Comment on the morphology of the erythrocytes.
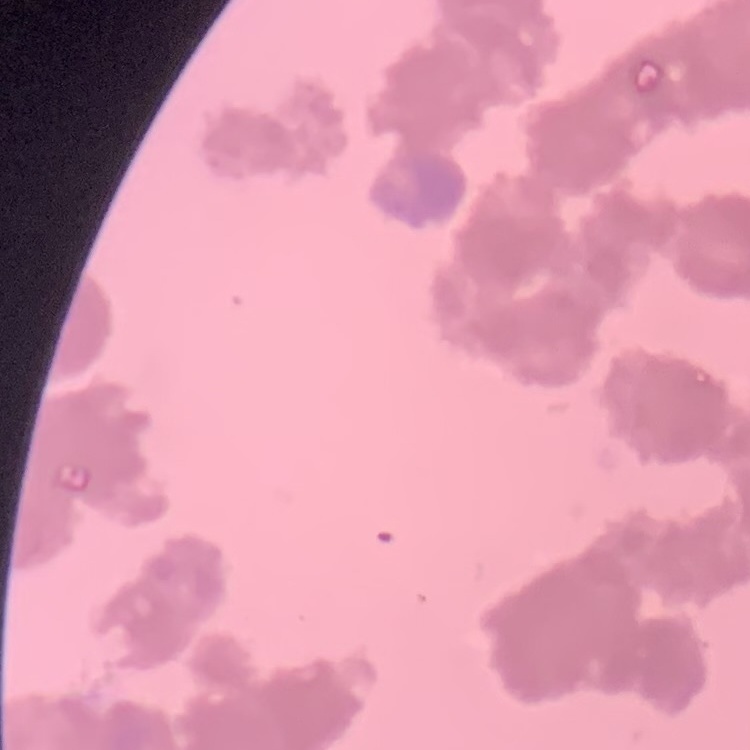
They show rouleaux formation.

Square crop of a larger photomicrograph. Thin peripheral smear. Stained with either Field's or Giemsa.